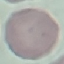

malaria_status: uninfected
image_type: cell patch, automatically extracted from a larger field of view and resized to 64 × 64 pixels
preparation: thin blood film
capture: smartphone camera at the microscope eyepiece
stain: Giemsa